Assess this cell for malaria.
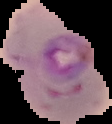

Parasitized.

image type = cell region segmented out of the field of view; surrounding area masked to black
image size = 112×124 pixels
preparation = thin blood film